Assess for Plasmodium parasites.
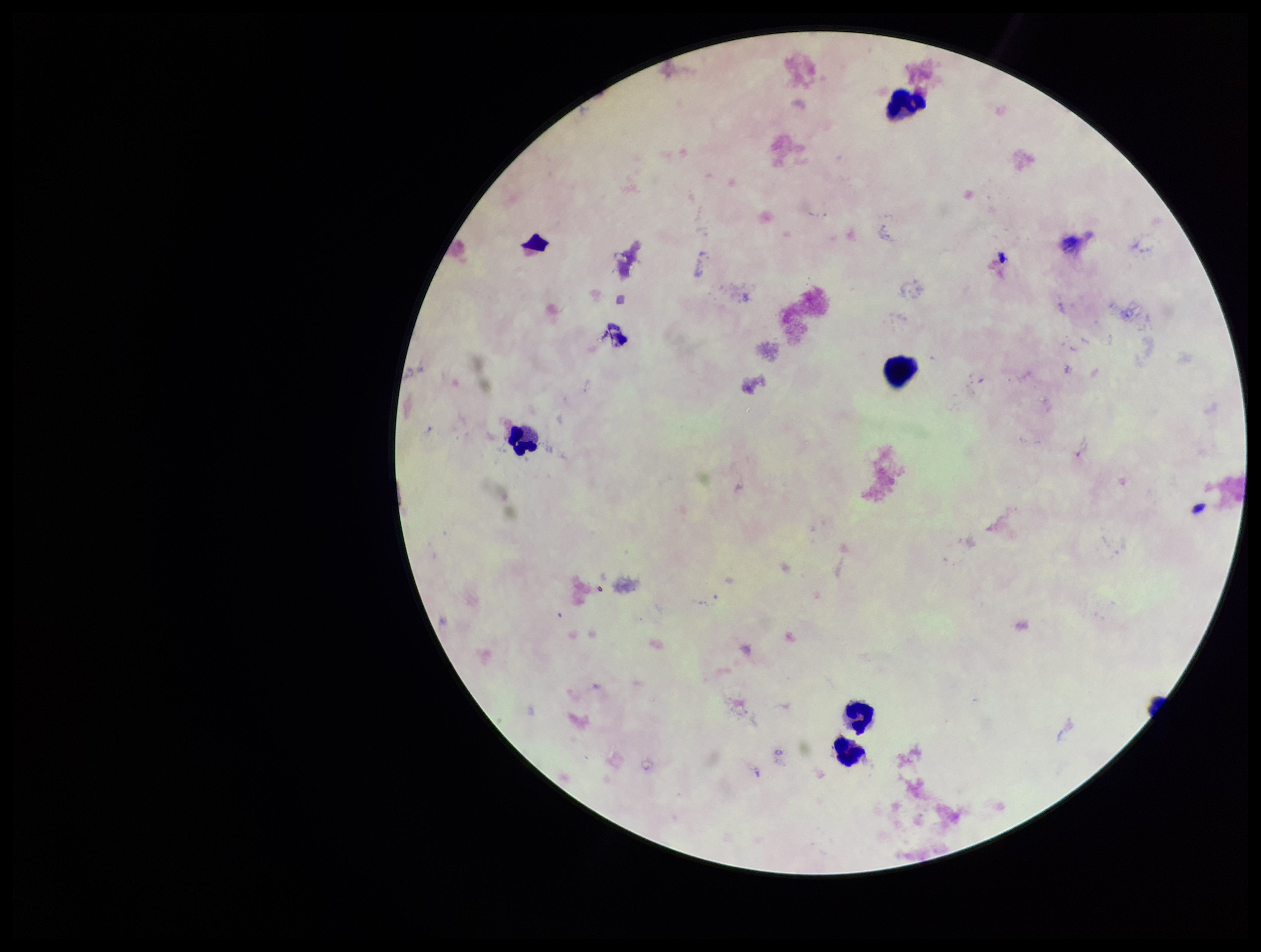
None detected.

species_reported_for_this_patient: Plasmodium falciparum
preparation: thick smear
patient_malaria_status: positive
capture: smartphone photograph through the microscope eyepiece
image_size: 1261×952 pixels
leukocyte_count: 4
parasite_count: 0
field_of_view: one from this slide
stain: Giemsa